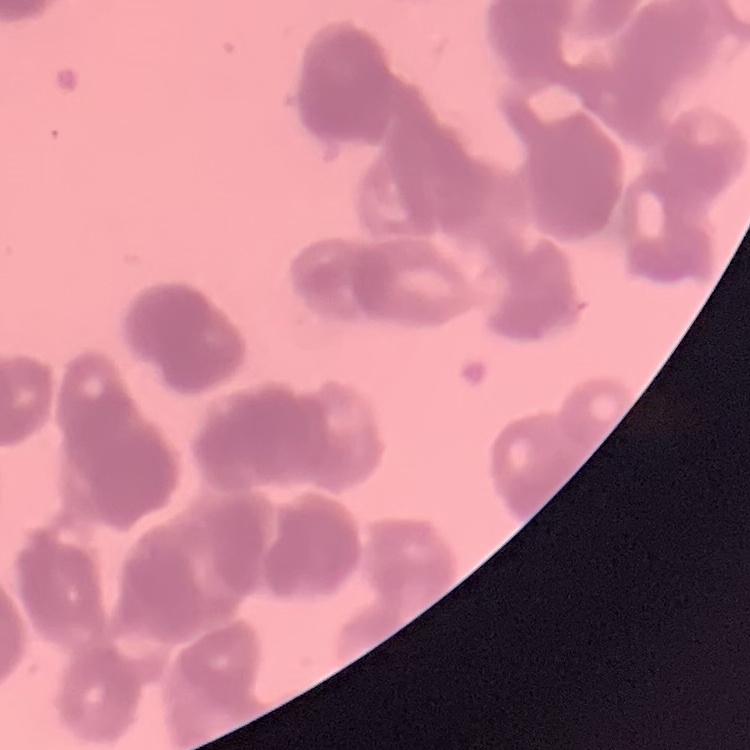
Summary:
  - Red blood cell morphology: rouleaux formation
  - Preparation: thin blood smear
  - Image type: one tile cut from a larger photomicrograph
  - Stain: Field's or Giemsa